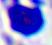

{
  "magnification": "400x",
  "modality": "photomicrograph",
  "identification": "leukocyte"
}